Identify the parasite.
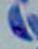
This is Toxoplasma gondii.

Summary:
  - Modality: photomicrograph
  - Magnification: 1000x